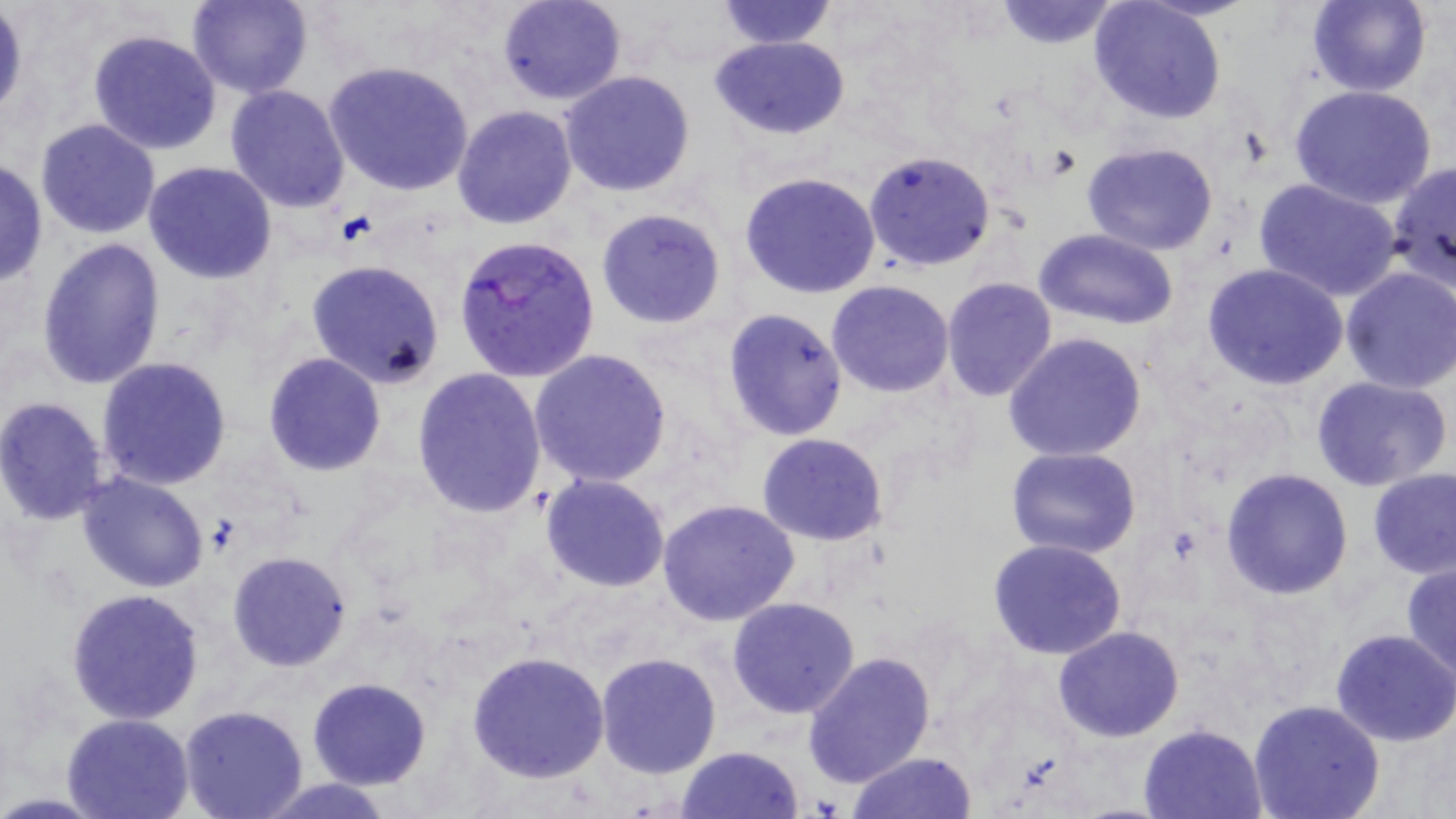
slide_level_diagnosis: Plasmodium falciparum
uninfected_red_blood_cell_locations: 'approximate bounding boxes as named x1/y1/x2/y2 corners in pixels: (x1=186, y1=0, x2=313, y2=98), (x1=498, y1=0, x2=627, y2=105), (x1=712, y1=0, x2=839, y2=50), (x1=993, y1=0, x2=1121, y2=49), (x1=1089, y1=0, x2=1226, y2=123), (x1=1307, y1=0, x2=1431, y2=97), (x1=0, y1=7, x2=27, y2=123), (x1=88, y1=29, x2=222, y2=155), (x1=711, y1=35, x2=850, y2=141), (x1=326, y1=61, x2=475, y2=197), (x1=558, y1=71, x2=696, y2=195), (x1=223, y1=84, x2=350, y2=214), (x1=1291, y1=86, x2=1436, y2=209), (x1=451, y1=105, x2=578, y2=229), (x1=34, y1=118, x2=162, y2=240), (x1=1082, y1=142, x2=1220, y2=255), (x1=863, y1=151, x2=996, y2=271), (x1=0, y1=159, x2=48, y2=287), (x1=1388, y1=159, x2=1456, y2=289), (x1=143, y1=161, x2=276, y2=284), (x1=739, y1=171, x2=882, y2=300), (x1=1253, y1=178, x2=1403, y2=302), (x1=595, y1=207, x2=727, y2=330), (x1=1036, y1=228, x2=1177, y2=328), (x1=36, y1=237, x2=166, y2=390), (x1=305, y1=260, x2=446, y2=387), (x1=1202, y1=263, x2=1350, y2=391), (x1=1338, y1=266, x2=1456, y2=393), (x1=942, y1=277, x2=1057, y2=401), (x1=826, y1=280, x2=954, y2=397), (x1=720, y1=308, x2=849, y2=440), (x1=1004, y1=333, x2=1147, y2=461), (x1=528, y1=349, x2=672, y2=489), (x1=262, y1=353, x2=385, y2=476), (x1=97, y1=356, x2=231, y2=491), (x1=410, y1=367, x2=547, y2=519), (x1=1312, y1=376, x2=1453, y2=494), (x1=0, y1=396, x2=111, y2=526), (x1=756, y1=433, x2=889, y2=546), (x1=1006, y1=447, x2=1141, y2=560), (x1=1221, y1=468, x2=1353, y2=598), (x1=1368, y1=469, x2=1456, y2=580), (x1=76, y1=472, x2=209, y2=593), (x1=539, y1=474, x2=669, y2=592), (x1=657, y1=498, x2=803, y2=628), (x1=987, y1=539, x2=1128, y2=660), (x1=226, y1=552, x2=351, y2=671), (x1=1400, y1=560, x2=1456, y2=681), (x1=66, y1=588, x2=205, y2=725), (x1=727, y1=597, x2=861, y2=718), (x1=1053, y1=626, x2=1185, y2=742), (x1=1331, y1=629, x2=1456, y2=747), (x1=467, y1=648, x2=609, y2=782), (x1=595, y1=651, x2=723, y2=778), (x1=802, y1=652, x2=935, y2=789), (x1=307, y1=677, x2=432, y2=789), (x1=1247, y1=699, x2=1386, y2=819), (x1=178, y1=704, x2=309, y2=819), (x1=62, y1=713, x2=194, y2=819), (x1=1138, y1=724, x2=1267, y2=819), (x1=677, y1=745, x2=803, y2=819), (x1=847, y1=751, x2=979, y2=819), (x1=254, y1=778, x2=400, y2=818)'
stain: May-Grünwald-Giemsa
preparation: thin blood smear
image_size: 1456×819 pixels
modality: light microscopy
plasmodium_falciparum_infected_red_blood_cell_locations: 'approximate bounding boxes as named x1/y1/x2/y2 corners in pixels: (x1=453, y1=234, x2=600, y2=385)'
magnification: 1000x
field_of_view: one of a larger specimen